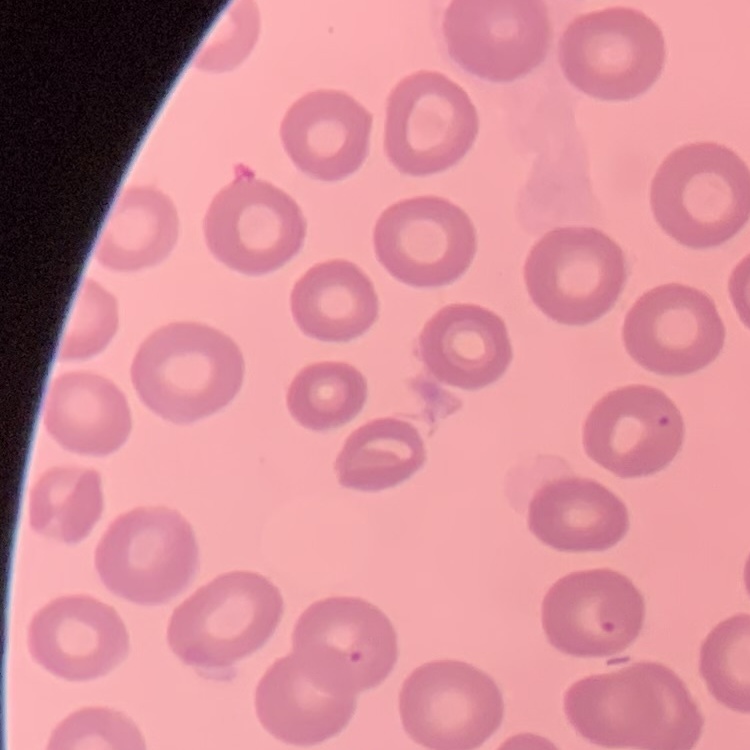
{
  "erythrocyte_morphology": "no rouleaux formation",
  "preparation": "thin peripheral smear",
  "stain": "Field's or Giemsa",
  "image_type": "square crop of a larger photomicrograph"
}